State which parasite is depicted.
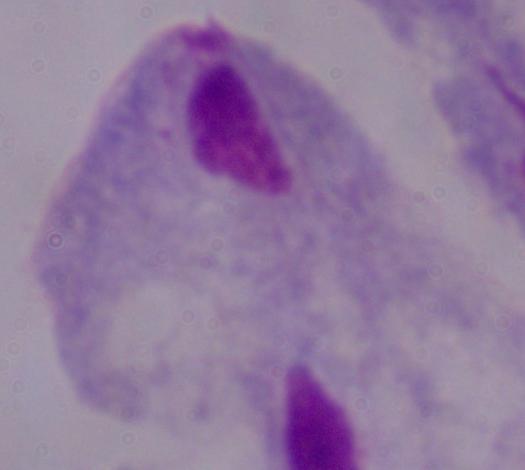

A trichomonad.

modality = micrograph
magnification = 1000x